Identify the blood parasite species.
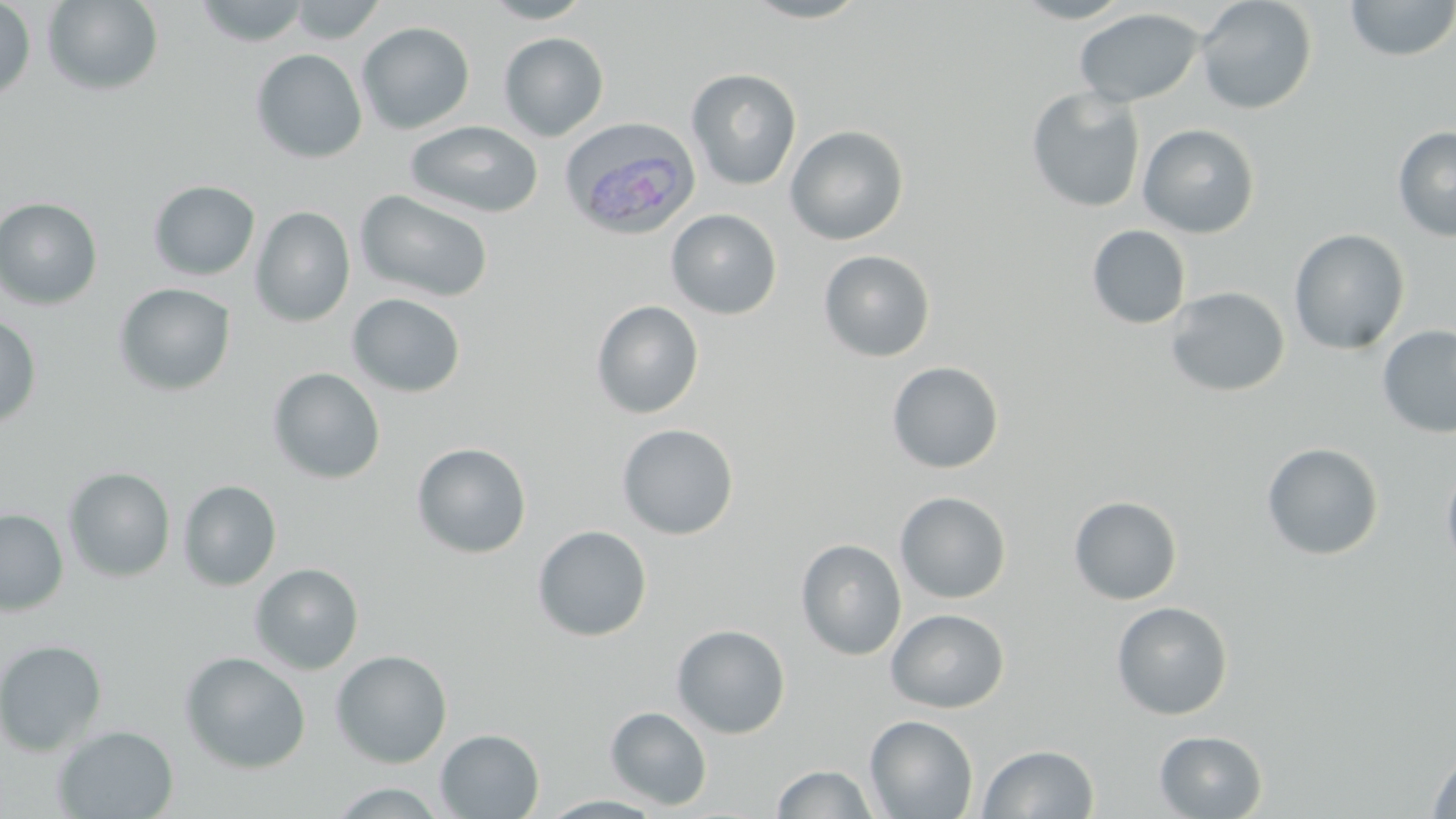
Plasmodium ovale.

{
  "modality": "optical microscopy",
  "field_of_view": "one of a larger specimen",
  "plasmodium_ovale_infected_red_blood_cell_locations": "approximate bounding boxes as (x1,y1)-(x2,y2) corner pairs in pixels: (560,119)-(703,241)",
  "image_size": "1456×819 pixels",
  "uninfected_red_blood_cell_locations": "approximate bounding boxes as (x1,y1)-(x2,y2) corner pairs in pixels: (193,0)-(311,46), (288,0)-(386,43), (481,0)-(594,23), (741,0)-(873,23), (1010,0)-(1137,23), (1195,0)-(1318,115), (1344,0)-(1456,61), (0,1)-(36,104), (42,1)-(163,96), (1074,8)-(1204,107), (357,22)-(475,134), (498,33)-(609,141), (250,49)-(367,163), (685,68)-(802,191), (1026,87)-(1146,213), (405,120)-(544,218), (1138,123)-(1260,238), (785,125)-(909,245), (1392,126)-(1456,243), (148,180)-(261,281), (354,189)-(494,303), (0,197)-(103,310), (250,206)-(355,327), (665,209)-(782,319), (1087,225)-(1191,329), (1288,228)-(1411,355), (818,250)-(936,363), (113,283)-(236,396), (1164,286)-(1290,398), (347,293)-(466,398), (590,300)-(705,419), (0,314)-(42,430), (1376,325)-(1456,439), (886,361)-(1004,474), (267,367)-(386,485), (616,423)-(739,540), (411,442)-(532,559), (1261,442)-(1384,560), (1441,458)-(1456,578), (63,467)-(176,582), (178,480)-(282,591), (894,491)-(1012,604), (1068,495)-(1182,605), (0,508)-(69,616), (532,525)-(653,642), (796,538)-(907,661), (249,563)-(364,675), (1111,601)-(1233,720), (885,608)-(1010,713), (671,624)-(791,738), (0,639)-(107,756), (330,650)-(452,769), (179,651)-(311,774), (605,706)-(712,811), (865,715)-(978,819), (52,725)-(179,818), (435,728)-(545,818), (1154,730)-(1268,818), (978,744)-(1099,818), (1426,749)-(1456,818), (771,764)-(879,819), (327,783)-(450,817), (539,795)-(668,818)",
  "magnification": "1000x",
  "stain": "May-Grünwald-Giemsa",
  "preparation": "thin blood film"
}